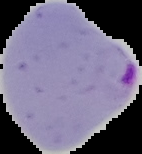

Summary:
  - Malaria status: parasitized
  - Image type: segmented cell region on a black background
  - Preparation: thin blood smear
  - Image size: 142×154 pixels